Classify this cell by malaria status.
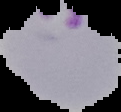
Parasitized.

Summary:
  - Image size: 121×112 pixels
  - Preparation: thin blood film
  - Image type: segmented cell region on a black background